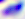
identification = Toxoplasma gondii
magnification = 400x
modality = micrograph